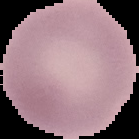

image type = segmented cell region on a black background
result = negative for malaria parasites
image size = 139×139 pixels
preparation = thin blood film